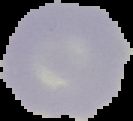

Summary:
  - Preparation: thin blood film
  - Result: no Plasmodium parasites seen
  - Image type: cell region segmented out of the field of view; surrounding area masked to black
  - Image size: 133×121 pixels